Describe the morphology of the erythrocytes.
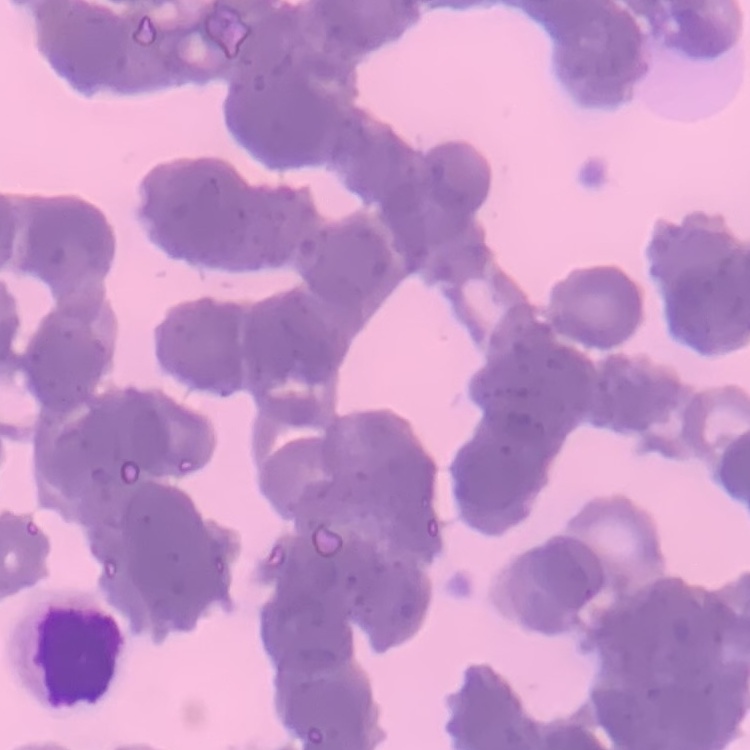
They show rouleaux formation.

Thin blood smear. Stained with either Field's or Giemsa. One tile cut from a larger photomicrograph.